Report the malaria status of this cell.
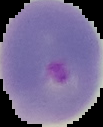

It is parasitized.

The area outside the segmented cell region is set to black. From a thin blood smear. Image is 103×127 pixels.